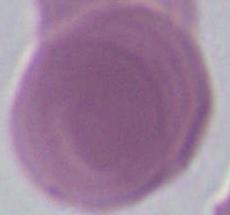
Captured at 1000x magnification. An erythrocyte is shown. Micrograph.